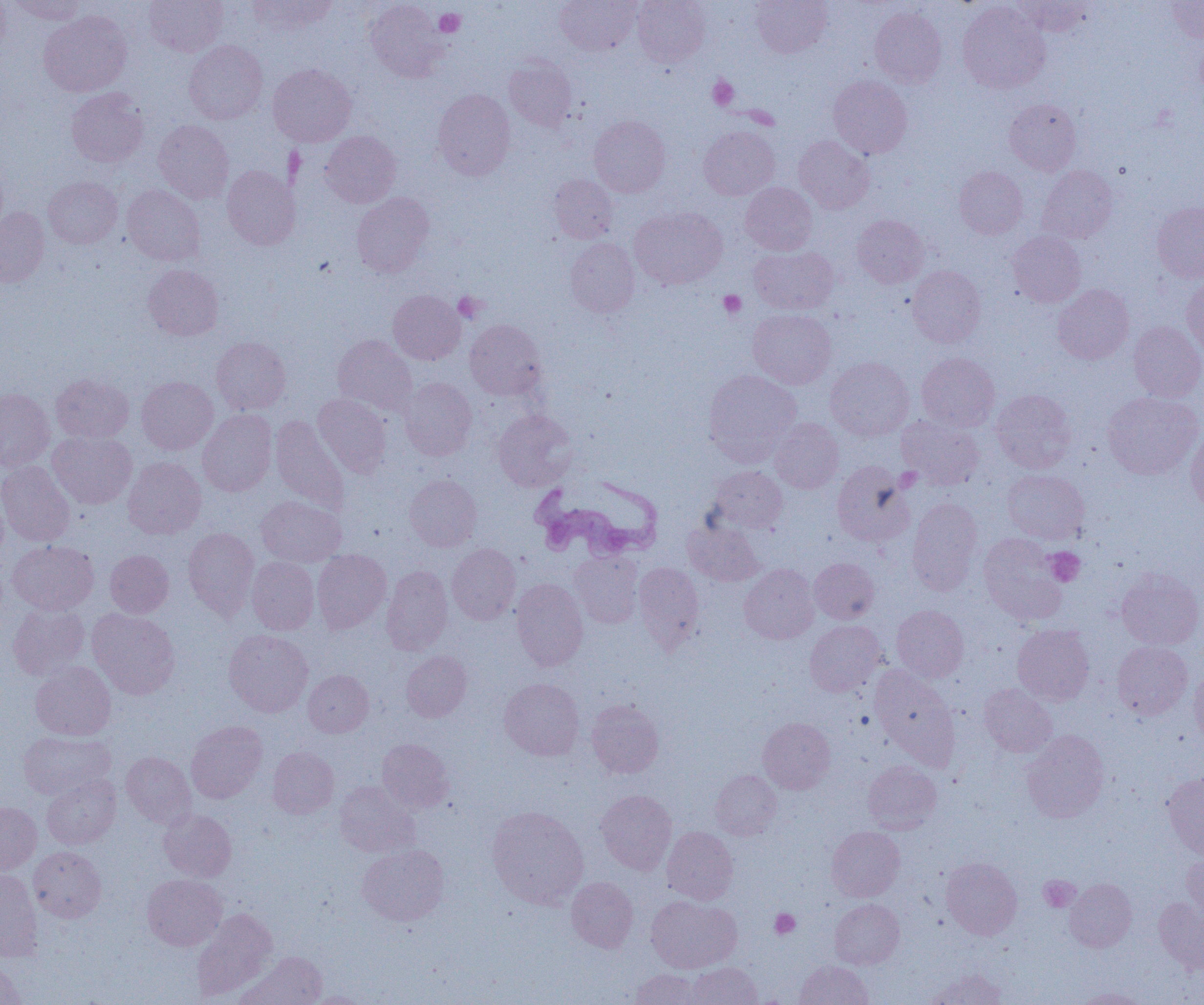

Summary:
  - Coordinate format: approximate bounding boxes as (x1,y1)-(x2,y2) corner pairs in pixels
  - Trypanosoma brucei locations: (531,474)-(662,561)
  - Uninfected red blood cell locations: (0,0)-(10,59), (8,0)-(87,24), (144,0)-(228,56), (248,0)-(336,35), (555,0)-(641,55), (632,0)-(711,67), (751,0)-(831,57), (1013,0)-(1095,36), (365,1)-(448,82), (1167,1)-(1204,43), (957,2)-(1050,94), (869,6)-(946,87), (38,11)-(131,96), (184,40)-(267,124), (504,57)-(578,132), (268,63)-(356,146), (828,75)-(912,158), (66,88)-(148,167), (433,89)-(515,180), (1004,99)-(1081,175), (589,115)-(670,197), (153,119)-(234,203), (699,126)-(780,200), (320,130)-(401,207), (794,135)-(874,214), (222,165)-(300,250), (1037,165)-(1118,243), (954,166)-(1027,239), (549,175)-(618,243), (44,176)-(122,248), (740,182)-(817,255), (122,184)-(205,266), (351,192)-(434,277), (1151,202)-(1204,282), (629,206)-(726,289), (0,207)-(49,287), (852,215)-(928,288), (1008,232)-(1085,308), (565,238)-(640,317), (749,245)-(839,315), (143,264)-(223,341), (907,266)-(986,347), (1181,276)-(1204,359), (1052,284)-(1133,364), (388,290)-(465,364), (748,309)-(836,389), (465,319)-(547,400), (1129,320)-(1204,401), (333,334)-(417,417), (211,336)-(290,414), (917,353)-(1000,431), (825,357)-(914,441), (704,369)-(801,464), (50,374)-(133,443), (136,377)-(218,454), (400,377)-(477,460), (0,388)-(54,471), (991,389)-(1077,473), (1102,392)-(1202,479), (313,394)-(392,477), (198,409)-(277,496), (493,409)-(578,491), (897,414)-(984,490), (270,416)-(350,514), (768,418)-(843,493), (1185,426)-(1204,514), (47,431)-(137,508), (123,457)-(206,539), (0,461)-(75,547), (832,461)-(914,546), (709,466)-(787,533), (1002,469)-(1089,544), (405,474)-(481,551), (0,481)-(9,562), (256,496)-(345,566), (908,498)-(983,595), (684,518)-(763,586), (183,527)-(259,619), (979,533)-(1067,624), (8,540)-(98,615), (447,543)-(520,624), (312,549)-(391,633), (105,550)-(174,617), (570,551)-(643,628), (247,557)-(319,634), (809,558)-(878,624), (633,562)-(704,652), (739,564)-(819,644), (381,565)-(453,655), (1116,568)-(1204,649), (511,578)-(588,671), (8,603)-(90,680), (891,605)-(968,682), (87,608)-(180,699), (805,620)-(886,696), (1012,623)-(1095,705), (224,629)-(313,717), (1112,641)-(1193,720), (401,651)-(472,721), (30,662)-(116,740), (869,666)-(957,764), (1189,667)-(1204,748), (303,669)-(373,737), (500,678)-(584,761), (979,685)-(1057,757), (586,699)-(664,777), (759,717)-(836,793), (186,721)-(267,803), (18,730)-(115,800), (1022,730)-(1109,822), (377,738)-(454,813), (268,746)-(339,818), (121,751)-(196,828), (863,761)-(941,833), (710,770)-(781,840), (1163,772)-(1204,859), (42,775)-(121,849), (334,781)-(420,857), (596,789)-(677,875), (0,801)-(42,874), (487,806)-(589,909), (159,808)-(237,881), (826,826)-(905,901), (662,827)-(738,904), (357,843)-(449,925), (29,846)-(106,922), (1181,853)-(1204,922), (941,857)-(1022,939), (0,870)-(43,961), (142,874)-(226,951), (567,877)-(638,952), (1064,878)-(1137,952), (646,896)-(741,973), (830,898)-(904,968), (1153,898)-(1204,972), (192,910)-(277,1001), (238,952)-(327,1005), (794,960)-(872,1005), (0,962)-(26,1005), (689,962)-(761,1005), (630,969)-(702,1004), (927,969)-(1006,1005), (1074,987)-(1149,1005), (301,991)-(375,1004)
  - Platelet locations: (434,9)-(465,37), (708,75)-(738,110), (719,290)-(746,318), (453,292)-(486,322), (1045,547)-(1085,586), (1039,875)-(1080,912), (770,909)-(800,939)
  - Slide-level diagnosis: Trypanosoma brucei
  - Preparation: thin blood film
  - Image size: 1204×1005 pixels
  - Field of view: one of a larger specimen
  - Modality: optical microscopy
  - Magnification: 1000x